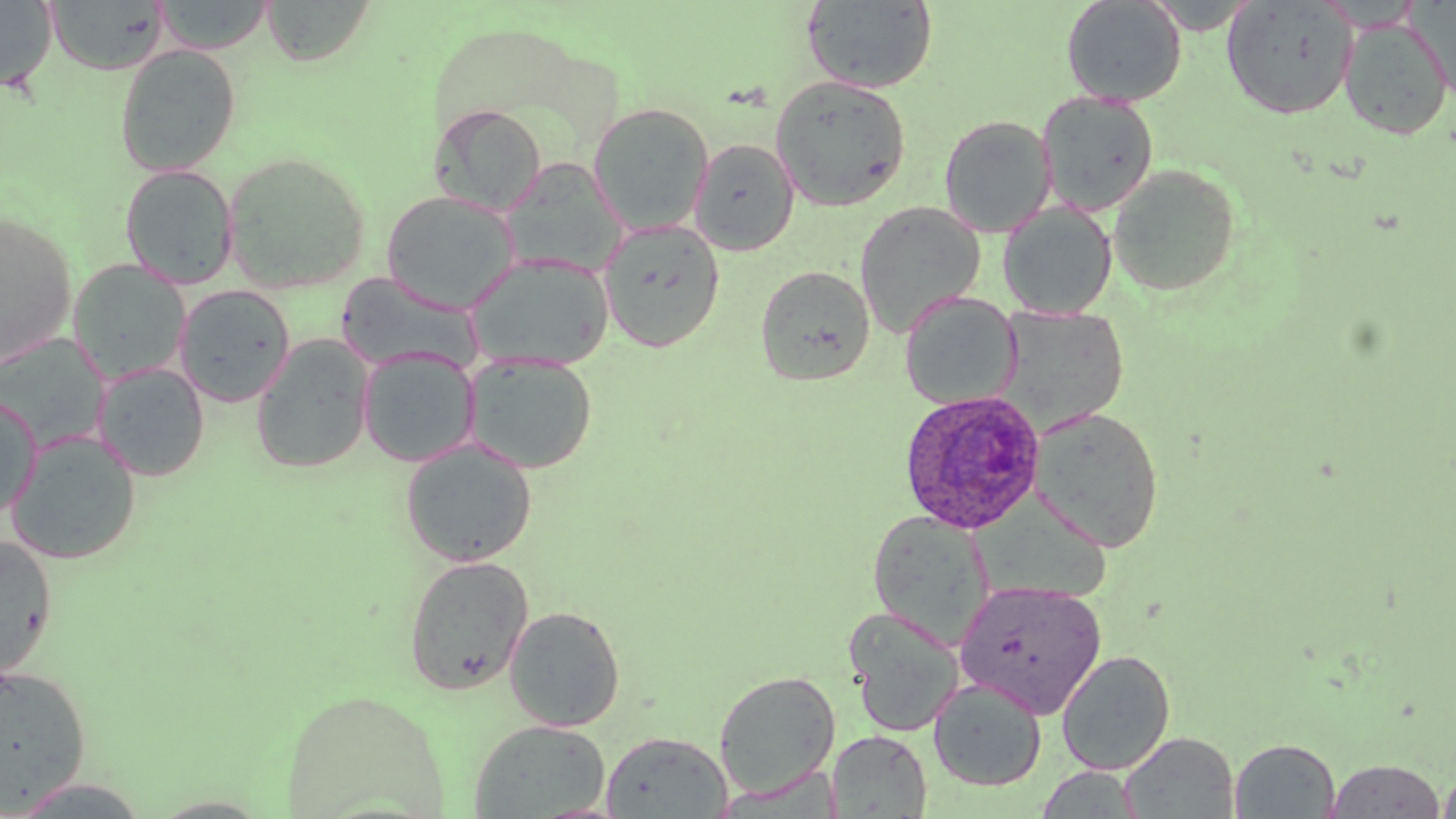

slide-level diagnosis = Plasmodium ovale
image size = 1456×819 pixels
field of view = single
modality = optical microscopy
Plasmodium ovale-infected red blood cell locations = approximate bounding boxes as named x1/y1/x2/y2 corners in pixels: (x1=897, y1=388, x2=1047, y2=534)
stain = May-Grünwald-Giemsa
magnification = 1000x
preparation = thin blood film
uninfected red blood cell locations = approximate bounding boxes as named x1/y1/x2/y2 corners in pixels: (x1=0, y1=0, x2=58, y2=92), (x1=45, y1=0, x2=169, y2=74), (x1=153, y1=0, x2=275, y2=53), (x1=262, y1=0, x2=375, y2=66), (x1=802, y1=0, x2=938, y2=93), (x1=1061, y1=0, x2=1187, y2=106), (x1=1221, y1=1, x2=1357, y2=120), (x1=1338, y1=18, x2=1453, y2=140), (x1=114, y1=44, x2=241, y2=176), (x1=770, y1=75, x2=910, y2=212), (x1=1037, y1=92, x2=1159, y2=216), (x1=588, y1=102, x2=713, y2=235), (x1=429, y1=103, x2=548, y2=215), (x1=939, y1=114, x2=1056, y2=237), (x1=689, y1=138, x2=800, y2=255), (x1=222, y1=151, x2=371, y2=293), (x1=500, y1=159, x2=628, y2=277), (x1=1108, y1=163, x2=1242, y2=297), (x1=120, y1=164, x2=239, y2=290), (x1=381, y1=190, x2=520, y2=313), (x1=854, y1=200, x2=986, y2=338), (x1=998, y1=202, x2=1117, y2=319), (x1=0, y1=210, x2=77, y2=368), (x1=598, y1=218, x2=726, y2=353), (x1=464, y1=253, x2=615, y2=371), (x1=68, y1=260, x2=190, y2=385), (x1=755, y1=265, x2=875, y2=387), (x1=335, y1=272, x2=483, y2=374), (x1=174, y1=284, x2=295, y2=408), (x1=899, y1=293, x2=1020, y2=410), (x1=994, y1=306, x2=1128, y2=436), (x1=250, y1=335, x2=375, y2=474), (x1=358, y1=348, x2=479, y2=467), (x1=464, y1=353, x2=598, y2=474), (x1=93, y1=362, x2=210, y2=481), (x1=0, y1=393, x2=41, y2=521), (x1=1029, y1=406, x2=1165, y2=553), (x1=5, y1=430, x2=142, y2=564), (x1=400, y1=438, x2=537, y2=567), (x1=976, y1=495, x2=1117, y2=608), (x1=867, y1=510, x2=994, y2=647), (x1=0, y1=535, x2=58, y2=678), (x1=403, y1=554, x2=534, y2=695), (x1=955, y1=580, x2=1107, y2=717), (x1=503, y1=605, x2=626, y2=731), (x1=846, y1=609, x2=965, y2=737), (x1=1056, y1=650, x2=1176, y2=776), (x1=0, y1=663, x2=92, y2=811), (x1=714, y1=671, x2=841, y2=799), (x1=928, y1=677, x2=1047, y2=792), (x1=281, y1=688, x2=450, y2=817), (x1=470, y1=719, x2=611, y2=817), (x1=600, y1=730, x2=733, y2=818), (x1=828, y1=730, x2=932, y2=818), (x1=1119, y1=731, x2=1240, y2=818), (x1=1230, y1=738, x2=1340, y2=818), (x1=1324, y1=758, x2=1448, y2=818), (x1=1037, y1=766, x2=1142, y2=817), (x1=1438, y1=767, x2=1456, y2=818)